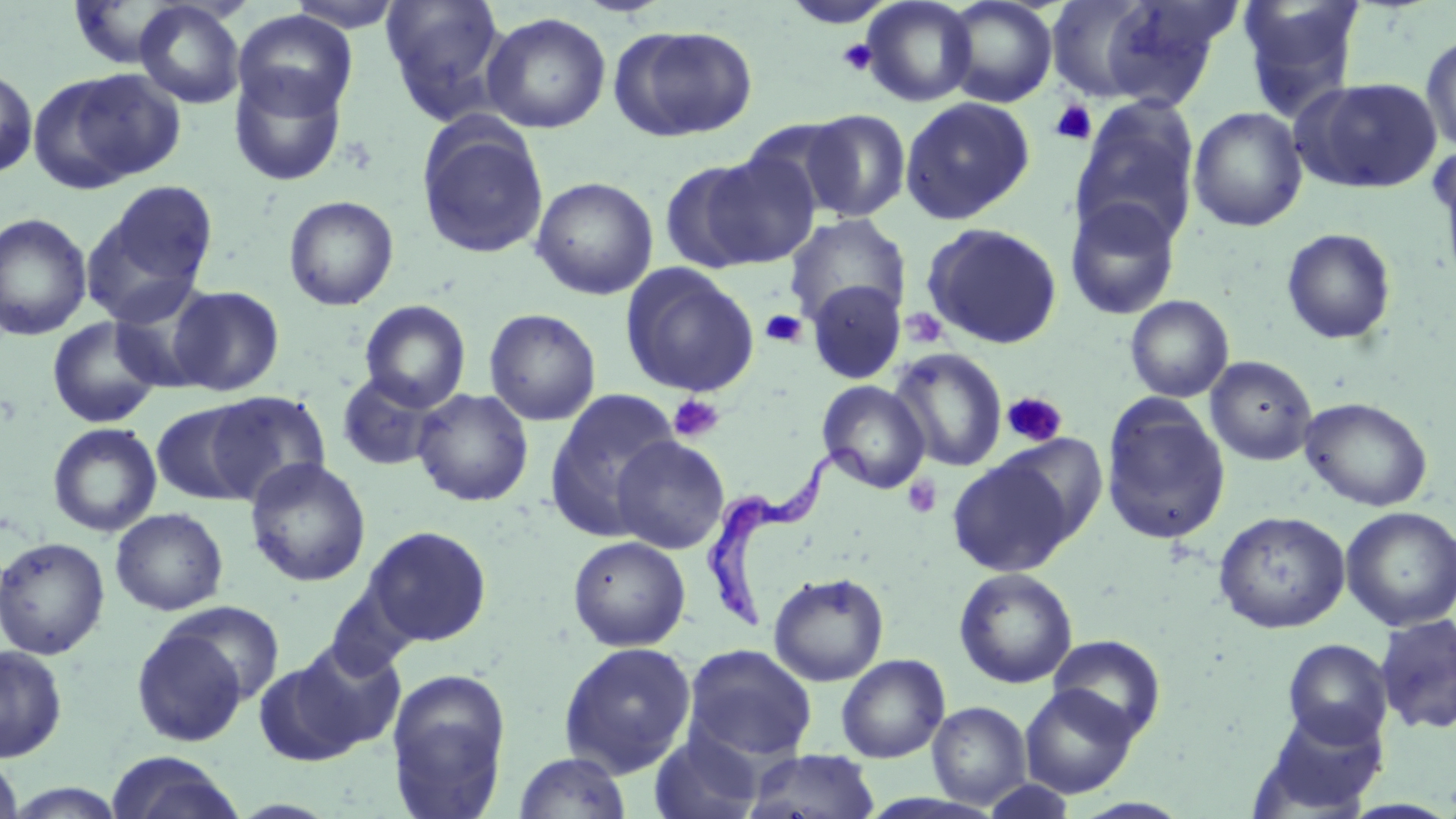
{
  "slide_level_diagnosis": "Trypanosoma brucei",
  "image_size": "1456×819 pixels",
  "preparation": "thin blood film",
  "field_of_view": "single",
  "magnification": "1000x",
  "stain": "May-Grünwald-Giemsa",
  "trypanosoma_brucei_locations": "approximate bounding boxes as [x1, y1, x2, y2] in pixels: [700, 442, 874, 631]",
  "modality": "optical microscopy",
  "platelet_locations": "approximate bounding boxes as [x1, y1, x2, y2] in pixels: [836, 39, 878, 76], [1049, 100, 1097, 146], [900, 307, 950, 350], [759, 309, 807, 349], [1001, 392, 1068, 448], [668, 394, 723, 443], [903, 475, 942, 518]",
  "uninfected_red_blood_cell_locations": "approximate bounding boxes as [x1, y1, x2, y2] in pixels: [285, 0, 407, 32], [381, 0, 509, 123], [782, 0, 897, 29], [861, 0, 978, 107], [942, 0, 1058, 108], [1042, 0, 1182, 104], [1095, 0, 1238, 109], [1237, 0, 1365, 120], [134, 1, 247, 109], [234, 10, 357, 121], [481, 12, 612, 134], [612, 25, 758, 141], [1420, 32, 1456, 154], [0, 66, 38, 180], [30, 69, 179, 190], [228, 69, 347, 187], [1292, 77, 1442, 194], [900, 96, 1035, 225], [1071, 99, 1200, 246], [1188, 107, 1308, 231], [800, 108, 911, 221], [741, 116, 855, 216], [417, 119, 549, 259], [1434, 146, 1456, 292], [659, 156, 783, 274], [530, 176, 658, 300], [86, 181, 218, 317], [283, 195, 399, 310], [1064, 197, 1181, 320], [0, 212, 93, 341], [785, 214, 911, 330], [922, 223, 1064, 349], [1281, 228, 1397, 345], [620, 264, 760, 398], [807, 280, 908, 383], [167, 285, 284, 396], [1125, 295, 1234, 402], [359, 300, 471, 412], [484, 308, 601, 425], [47, 317, 164, 429], [890, 347, 1007, 472], [1205, 356, 1317, 466], [336, 371, 443, 471], [817, 380, 930, 493], [411, 388, 534, 507], [206, 389, 332, 504], [545, 390, 680, 541], [1300, 397, 1433, 512], [1101, 399, 1231, 546], [151, 402, 260, 506], [48, 422, 162, 536], [997, 432, 1108, 544], [611, 435, 730, 554], [947, 455, 1075, 577], [245, 457, 371, 587], [1341, 506, 1455, 631], [111, 508, 228, 615], [1213, 510, 1350, 634], [363, 525, 492, 646], [568, 535, 691, 651], [0, 536, 110, 659], [954, 568, 1077, 689], [769, 572, 888, 686], [163, 600, 285, 704], [1374, 613, 1456, 735], [131, 625, 250, 746], [1049, 634, 1166, 742], [1283, 638, 1393, 747], [292, 639, 406, 751], [558, 641, 697, 777], [684, 644, 817, 761], [0, 645, 67, 762], [836, 654, 950, 763], [252, 657, 368, 767], [386, 669, 511, 818], [1019, 684, 1140, 798], [927, 701, 1031, 809], [1250, 705, 1389, 818], [648, 731, 763, 819], [743, 749, 880, 819], [512, 751, 632, 819], [106, 752, 246, 819], [0, 754, 23, 819], [4, 782, 129, 818]"
}